State which parasite is depicted.
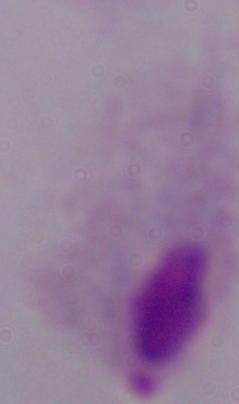

This is a trichomonad.

Captured at 1000x magnification. Micrograph.